Comment on the morphology of the red blood cells.
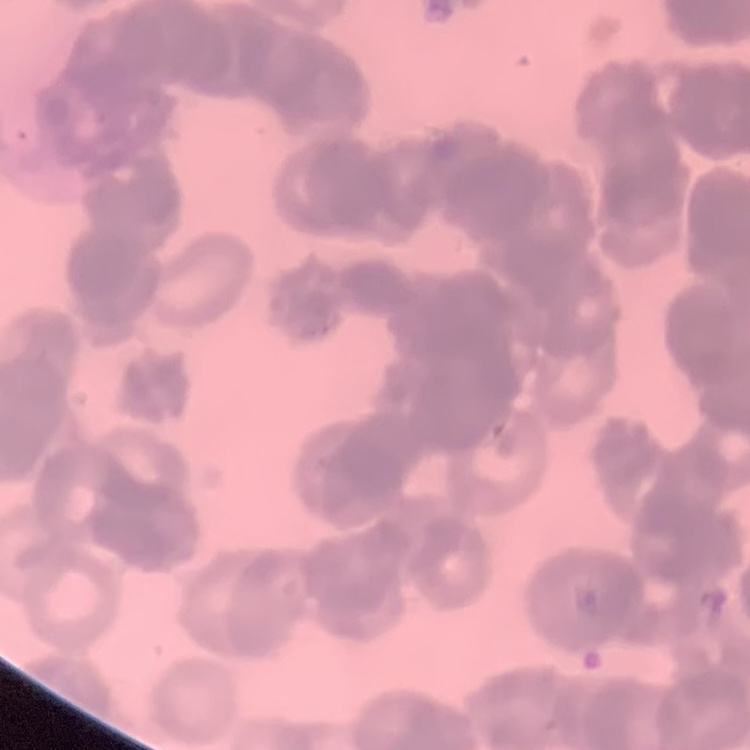

Rouleaux formation.

Thin blood film. One tile cut from a larger photomicrograph. Field's or Giemsa stain.